Locate and identify every blood parasite.
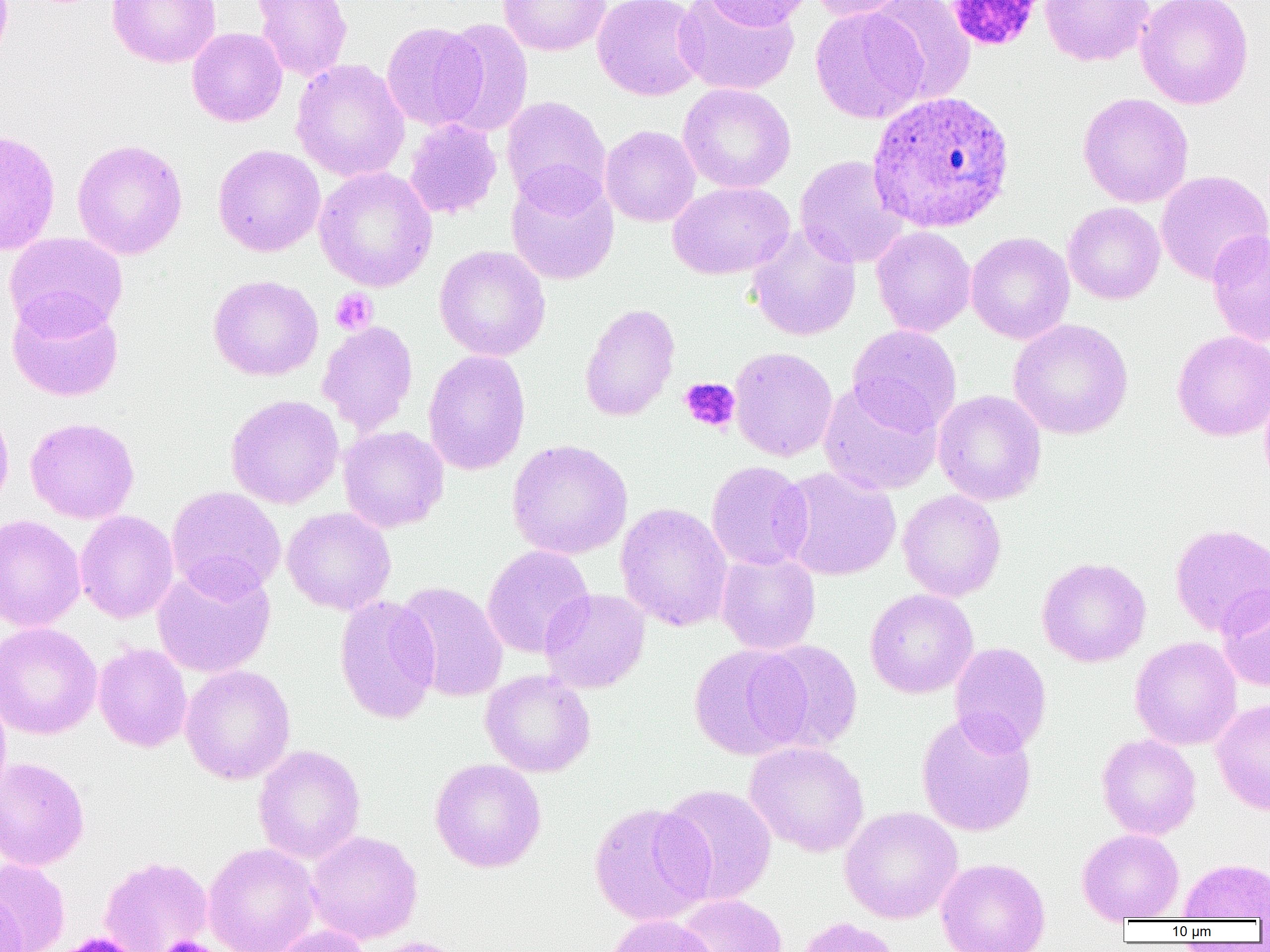
Approximate bounding boxes as (x1,y1)-(x2,y2) corner pairs in pixels.
Plasmodium ovale-infected red blood cells: (866,90)-(1015,234).
No Plasmodium falciparum, Plasmodium malariae, Plasmodium vivax, Babesia divergens, or Trypanosoma brucei observed.

Summary:
  - Uninfected red blood cell locations: (106,0)-(221,68), (251,0)-(352,82), (497,0)-(612,56), (592,0)-(707,101), (675,0)-(800,96), (703,0)-(811,31), (808,0)-(913,22), (1039,0)-(1155,66), (1135,0)-(1254,109), (866,1)-(976,103), (810,6)-(929,124), (436,18)-(534,138), (381,21)-(486,131), (187,27)-(287,127), (290,58)-(410,182), (678,83)-(796,193), (1077,93)-(1194,207), (501,96)-(611,211), (403,118)-(502,219), (600,125)-(701,227), (0,129)-(61,256), (71,139)-(188,260), (212,144)-(325,257), (795,155)-(910,268), (313,166)-(439,292), (506,170)-(619,285), (1155,170)-(1270,285), (668,180)-(794,280), (1062,190)-(1267,294), (1063,202)-(1165,304), (746,224)-(862,342), (871,226)-(976,337), (1206,228)-(1270,348), (5,231)-(128,336), (966,232)-(1074,344), (434,245)-(551,362), (208,274)-(324,381), (7,294)-(124,401), (579,302)-(680,422), (1008,319)-(1133,439), (317,320)-(418,436), (847,324)-(962,433), (1171,330)-(1270,441), (729,347)-(838,462), (423,350)-(531,475), (818,380)-(943,496), (1259,380)-(1270,494), (932,390)-(1046,506), (225,394)-(344,509), (0,404)-(15,515), (25,417)-(140,524), (338,425)-(449,533), (507,439)-(633,560), (706,460)-(813,572), (777,466)-(901,581), (166,486)-(286,600), (897,489)-(1006,602), (885,492)-(990,698), (615,502)-(733,632), (282,507)-(396,615), (74,510)-(179,623), (0,514)-(87,633), (1169,522)-(1270,637), (482,545)-(594,658), (715,552)-(821,655), (1036,556)-(1151,667), (152,562)-(276,678), (395,581)-(508,702), (1216,585)-(1270,691), (539,588)-(650,693), (865,588)-(978,699), (333,594)-(441,724), (0,622)-(102,740), (1130,636)-(1242,750), (753,639)-(864,753), (93,642)-(192,753), (949,642)-(1052,753), (688,644)-(809,760), (180,664)-(296,785), (480,670)-(596,777), (0,686)-(11,805), (1211,699)-(1270,814), (915,709)-(1037,838), (1097,734)-(1201,840), (745,741)-(869,857), (253,744)-(366,864), (0,757)-(90,871), (430,758)-(547,873), (657,783)-(777,905), (588,801)-(713,926), (839,806)-(963,924), (1077,829)-(1184,922), (305,830)-(423,944), (202,842)-(321,952), (98,855)-(213,952), (0,857)-(71,952), (935,857)-(1050,952), (1178,858)-(1270,920), (0,889)-(25,952), (675,894)-(788,952), (603,913)-(723,952), (795,917)-(901,952), (271,925)-(373,952), (363,936)-(470,952)
  - Platelet locations: (945,0)-(1045,52), (330,288)-(378,335), (680,377)-(740,434), (159,936)-(215,952)
  - Slide-level diagnosis: Plasmodium ovale
  - Image size: 1270×952 pixels
  - Field of view: one of a larger specimen
  - Magnification: 1000x
  - Preparation: thin blood smear
  - Modality: optical microscopy